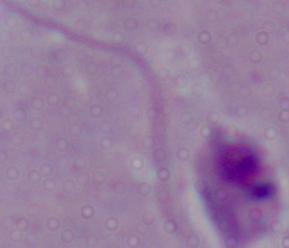
Summary:
  - Modality: photomicrograph
  - Identification: Leishmania
  - Magnification: 1000x